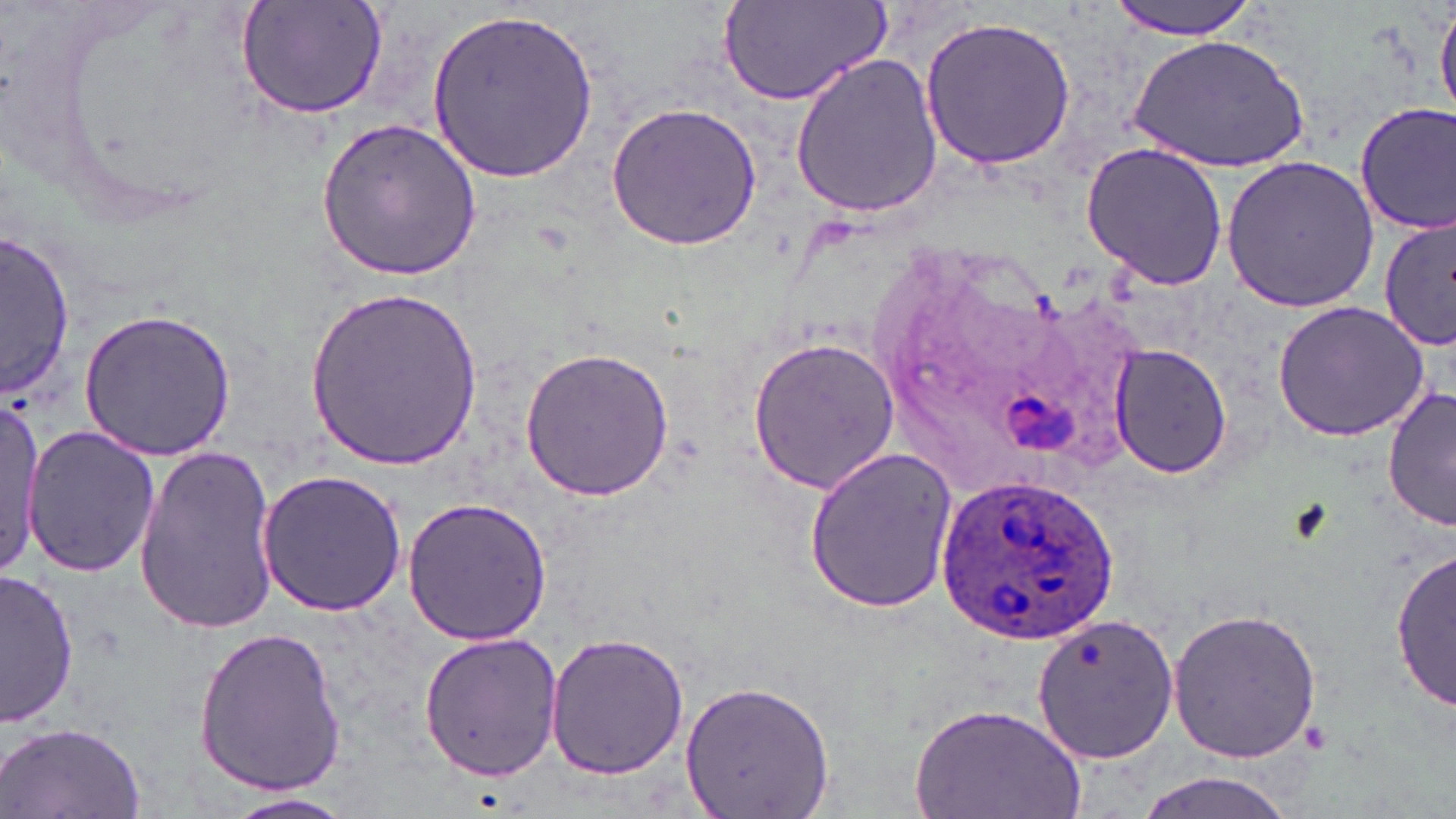
Summary:
  - Coordinate format: approximate bounding boxes as named x1/y1/x2/y2 corners in pixels
  - Plasmodium ovale-infected red blood cell locations: (x1=933, y1=468, x2=1120, y2=645)
  - Uninfected red blood cell locations: (x1=233, y1=0, x2=392, y2=119), (x1=1107, y1=0, x2=1263, y2=38), (x1=1434, y1=0, x2=1456, y2=121), (x1=722, y1=1, x2=888, y2=107), (x1=429, y1=5, x2=597, y2=184), (x1=919, y1=17, x2=1076, y2=168), (x1=1126, y1=31, x2=1316, y2=173), (x1=789, y1=53, x2=944, y2=218), (x1=606, y1=101, x2=763, y2=252), (x1=1355, y1=102, x2=1455, y2=236), (x1=317, y1=116, x2=481, y2=281), (x1=1080, y1=144, x2=1230, y2=291), (x1=1220, y1=155, x2=1384, y2=314), (x1=1379, y1=215, x2=1454, y2=351), (x1=3, y1=227, x2=77, y2=401), (x1=305, y1=286, x2=482, y2=470), (x1=1272, y1=300, x2=1433, y2=443), (x1=78, y1=308, x2=236, y2=459), (x1=746, y1=334, x2=901, y2=496), (x1=1106, y1=343, x2=1235, y2=481), (x1=518, y1=344, x2=674, y2=502), (x1=1384, y1=383, x2=1455, y2=533), (x1=0, y1=401, x2=44, y2=576), (x1=24, y1=425, x2=159, y2=578), (x1=135, y1=444, x2=281, y2=633), (x1=803, y1=446, x2=959, y2=613), (x1=256, y1=469, x2=408, y2=617), (x1=402, y1=495, x2=553, y2=647), (x1=1392, y1=547, x2=1454, y2=710), (x1=3, y1=568, x2=81, y2=726), (x1=1168, y1=606, x2=1324, y2=764), (x1=1032, y1=617, x2=1179, y2=765), (x1=190, y1=624, x2=346, y2=798), (x1=547, y1=631, x2=691, y2=781), (x1=417, y1=633, x2=565, y2=780), (x1=678, y1=682, x2=837, y2=817), (x1=912, y1=700, x2=1086, y2=819), (x1=1, y1=722, x2=149, y2=817), (x1=1129, y1=770, x2=1306, y2=819), (x1=223, y1=791, x2=358, y2=819)
  - Slide-level diagnosis: Plasmodium ovale
  - Modality: light microscopy
  - Stain: May-Grünwald-Giemsa
  - Image size: 1456×819 pixels
  - Magnification: 1000x
  - Preparation: thin blood film
  - Field of view: single